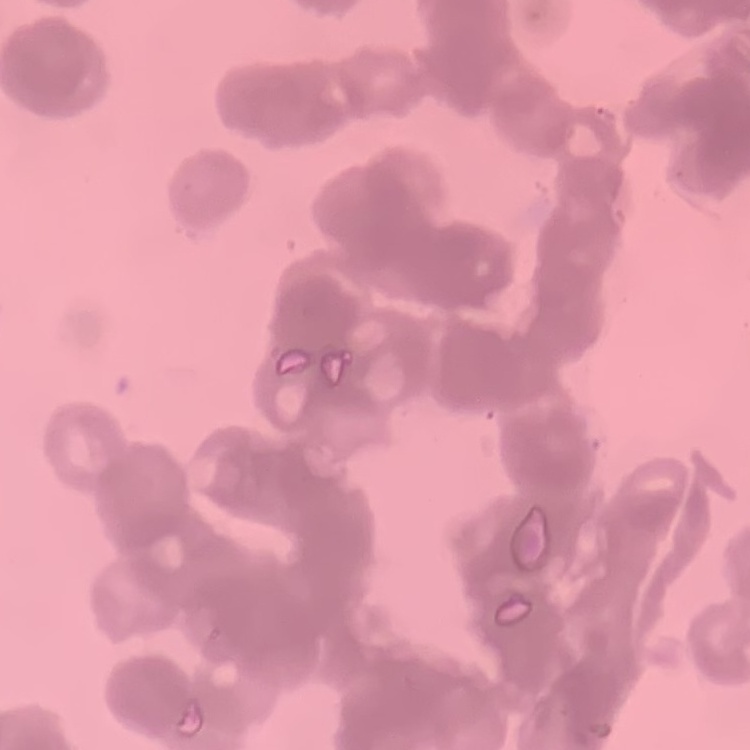

The red blood cells exhibit rouleaux formation. Field's or Giemsa stain. Square crop of a larger photomicrograph. Thin peripheral smear.